Describe the morphology of the red blood cells.
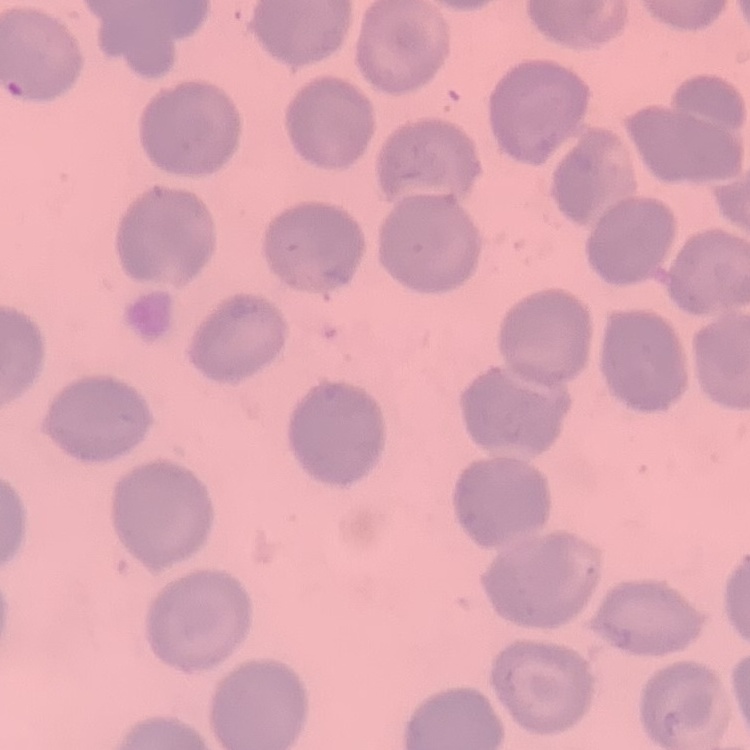
No rouleaux formation.

stain: Field's or Giemsa
preparation: thin blood film
image_type: one tile cut from a larger photomicrograph